State which parasite is depicted.
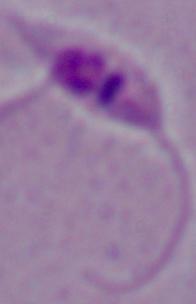
Leishmania.

magnification: 1000x
modality: micrograph